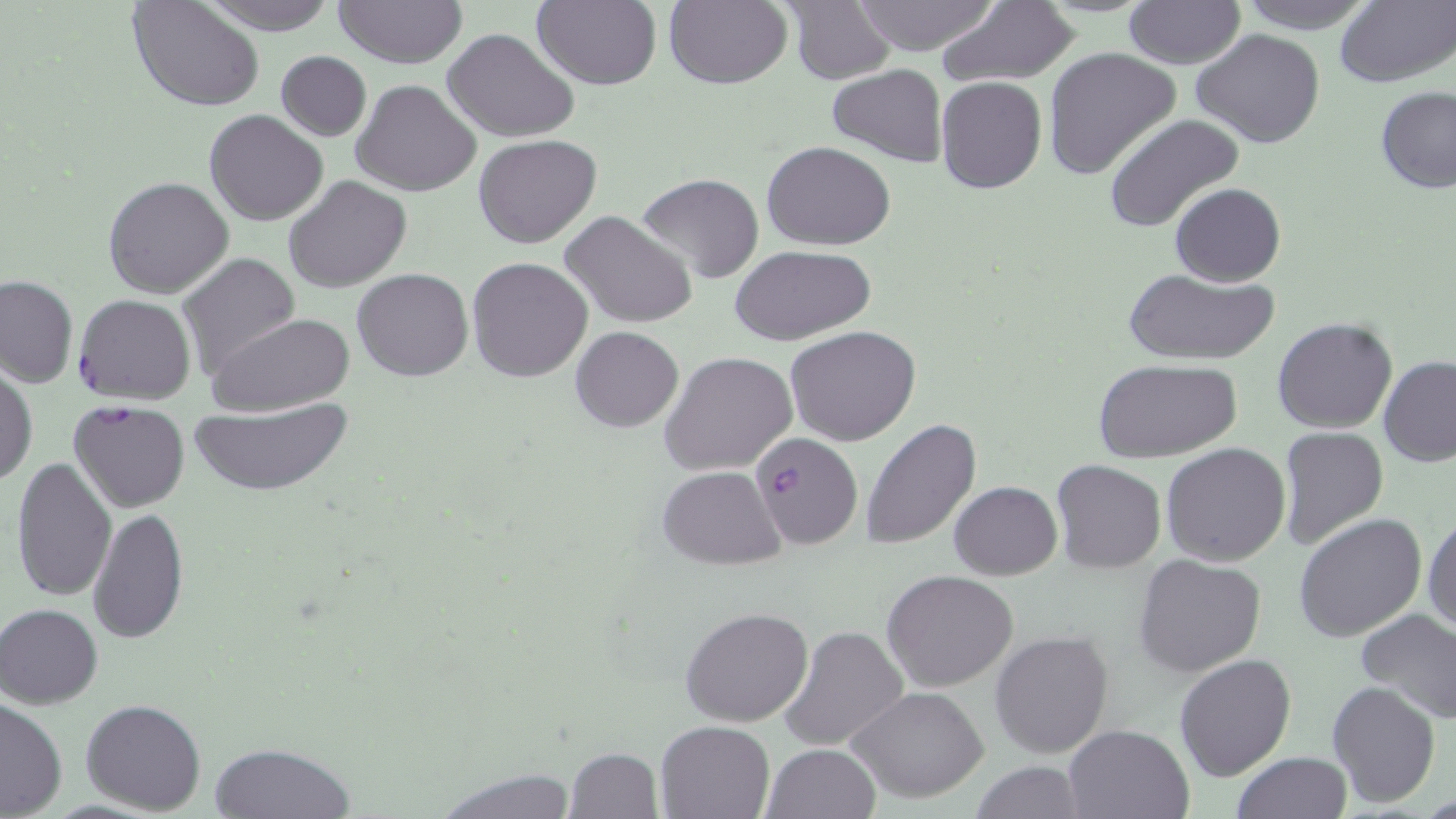
Summary:
  - Coordinate format: approximate bounding boxes as (x1, y1, x2, y2) in pixels
  - Uninfected red blood cell locations: (199, 0, 341, 35), (334, 0, 468, 68), (663, 0, 790, 90), (848, 0, 1007, 56), (1124, 0, 1245, 69), (1233, 0, 1374, 31), (1335, 0, 1455, 88), (129, 1, 263, 111), (531, 1, 661, 90), (782, 1, 898, 85), (937, 3, 1080, 86), (442, 27, 579, 143), (1192, 28, 1325, 147), (1043, 46, 1183, 181), (276, 51, 371, 141), (827, 65, 948, 166), (935, 76, 1046, 193), (352, 79, 481, 198), (1377, 87, 1456, 194), (204, 110, 327, 225), (1103, 114, 1245, 236), (474, 134, 601, 248), (761, 141, 897, 251), (634, 173, 766, 283), (104, 175, 234, 299), (284, 176, 411, 291), (1170, 183, 1286, 286), (560, 210, 698, 329), (729, 244, 876, 344), (176, 254, 302, 379), (467, 257, 594, 383), (354, 267, 472, 382), (1121, 267, 1281, 366), (0, 275, 76, 388), (207, 312, 353, 418), (1272, 317, 1398, 434), (570, 325, 683, 432), (785, 325, 921, 445), (660, 350, 797, 477), (1379, 356, 1456, 468), (1093, 358, 1243, 462), (1, 365, 36, 488), (189, 401, 353, 495), (861, 419, 982, 551), (1277, 427, 1390, 551), (1160, 443, 1291, 566), (10, 456, 117, 602), (1050, 461, 1166, 573), (657, 466, 786, 568), (949, 481, 1062, 581), (88, 508, 190, 646), (1423, 510, 1456, 636), (1294, 514, 1425, 644), (1133, 553, 1267, 678), (883, 569, 1021, 691), (1, 603, 102, 708), (680, 607, 814, 726), (1356, 609, 1456, 724), (780, 624, 910, 752), (989, 629, 1113, 759), (1174, 653, 1297, 781), (1326, 680, 1440, 807), (848, 685, 990, 802), (0, 699, 68, 818), (80, 699, 206, 815), (654, 719, 776, 819), (1063, 725, 1194, 818), (209, 741, 355, 818), (761, 743, 880, 819), (562, 748, 663, 818), (1231, 752, 1351, 819), (968, 761, 1091, 818), (431, 767, 579, 818)
  - Plasmodium falciparum-infected red blood cell locations: (73, 294, 196, 404), (68, 400, 192, 513), (752, 432, 863, 550)
  - Slide-level diagnosis: Plasmodium falciparum
  - Stain: May-Grünwald-Giemsa
  - Image size: 1456×819 pixels
  - Field of view: one of a larger specimen
  - Modality: optical microscopy
  - Magnification: 1000x
  - Preparation: thin blood smear